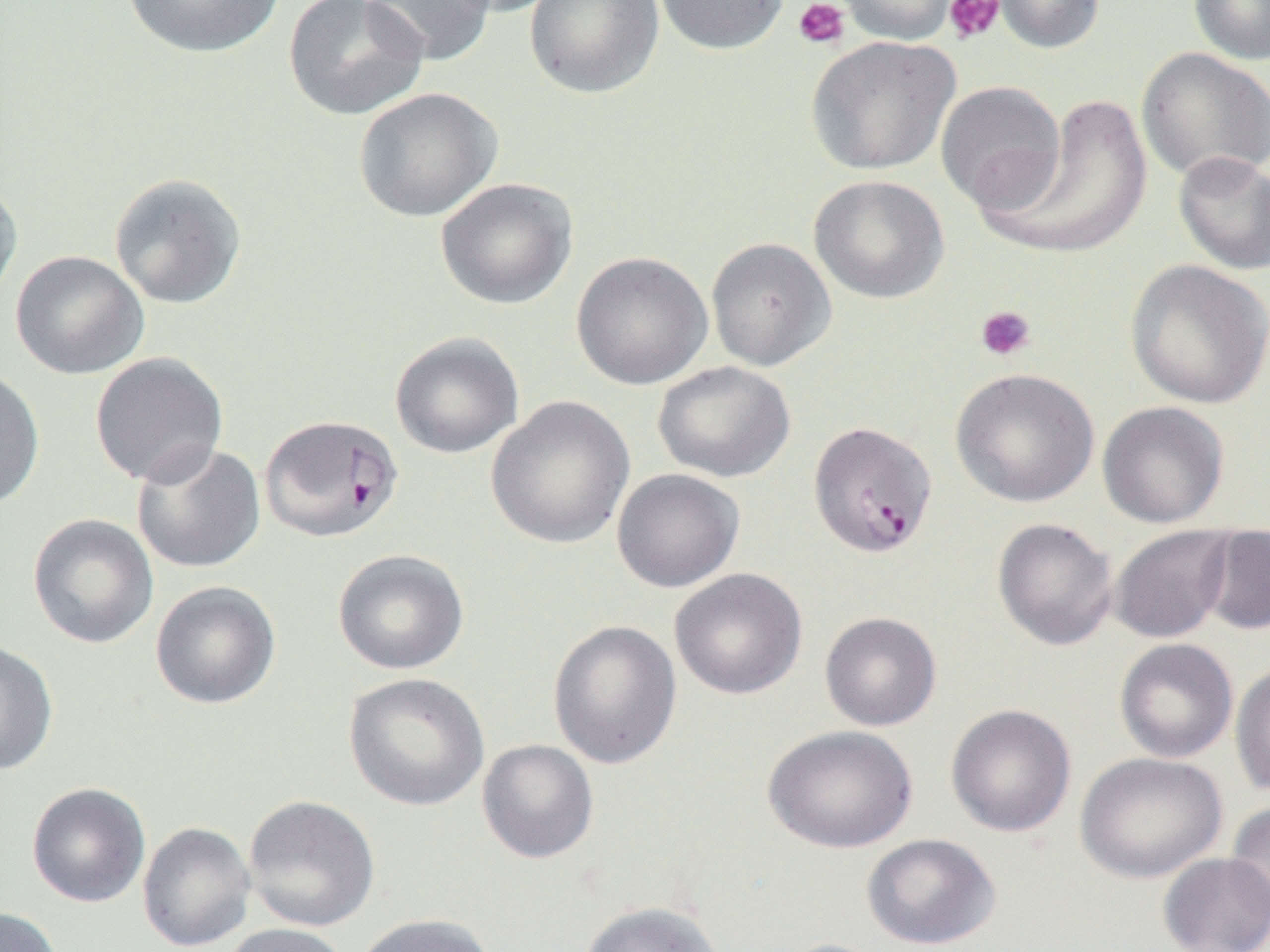

slide-level diagnosis = Plasmodium falciparum
field of view = one of a larger specimen
preparation = thin blood smear
magnification = 1000x
uninfected red blood cell locations = approximate bounding boxes as [x1, y1, x2, y2] in pixels: [119, 0, 285, 59], [283, 0, 429, 121], [360, 0, 497, 66], [437, 0, 566, 17], [524, 0, 664, 100], [653, 0, 790, 56], [833, 0, 961, 46], [992, 0, 1105, 54], [1188, 0, 1270, 65], [805, 35, 960, 176], [1137, 47, 1270, 184], [935, 80, 1066, 214], [353, 87, 502, 222], [981, 94, 1154, 260], [1172, 150, 1270, 275], [109, 173, 247, 309], [808, 174, 949, 304], [0, 177, 23, 308], [435, 178, 578, 309], [706, 237, 836, 371], [10, 250, 149, 380], [570, 251, 712, 390], [1124, 259, 1270, 409], [389, 331, 524, 459], [89, 352, 229, 487], [653, 361, 796, 482], [0, 367, 45, 511], [950, 367, 1100, 508], [485, 396, 635, 549], [1097, 401, 1230, 528], [131, 441, 266, 574], [612, 469, 745, 592], [27, 513, 159, 649], [991, 518, 1118, 651], [1108, 525, 1235, 644], [1200, 527, 1270, 635], [332, 549, 469, 675], [669, 568, 807, 700], [150, 581, 281, 710], [819, 611, 941, 731], [547, 619, 682, 769], [1114, 638, 1239, 763], [0, 639, 59, 775], [1230, 660, 1270, 797], [343, 672, 490, 811], [945, 704, 1077, 838], [763, 724, 918, 854], [476, 739, 599, 864], [1075, 751, 1227, 884], [26, 782, 151, 907], [243, 794, 381, 931], [1225, 802, 1270, 926], [136, 821, 256, 951], [861, 833, 1001, 950], [1157, 852, 1270, 952], [579, 900, 723, 952], [1, 906, 63, 952], [353, 913, 496, 952], [220, 923, 351, 952], [772, 938, 895, 952]
platelet locations = approximate bounding boxes as [x1, y1, x2, y2] in pixels: [793, 0, 850, 50], [943, 0, 1005, 45], [975, 304, 1037, 362]
modality = optical microscopy
Plasmodium falciparum-infected red blood cell locations = approximate bounding boxes as [x1, y1, x2, y2] in pixels: [255, 416, 399, 545], [814, 420, 943, 557]
image size = 1270×952 pixels